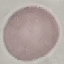
malaria status = uninfected
image type = cell patch, automatically extracted from a larger field of view and resized to 64 × 64 pixels
stain = Giemsa
capture = smartphone camera at the microscope eyepiece
preparation = thin blood film